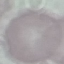
Malaria status: uninfected. Thin blood film. Acquired by smartphone through the microscope eyepiece. Automatically extracted cell patch, resized to 64 × 64 pixels. Giemsa-stained preparation.